Comment on the morphology of the erythrocytes.
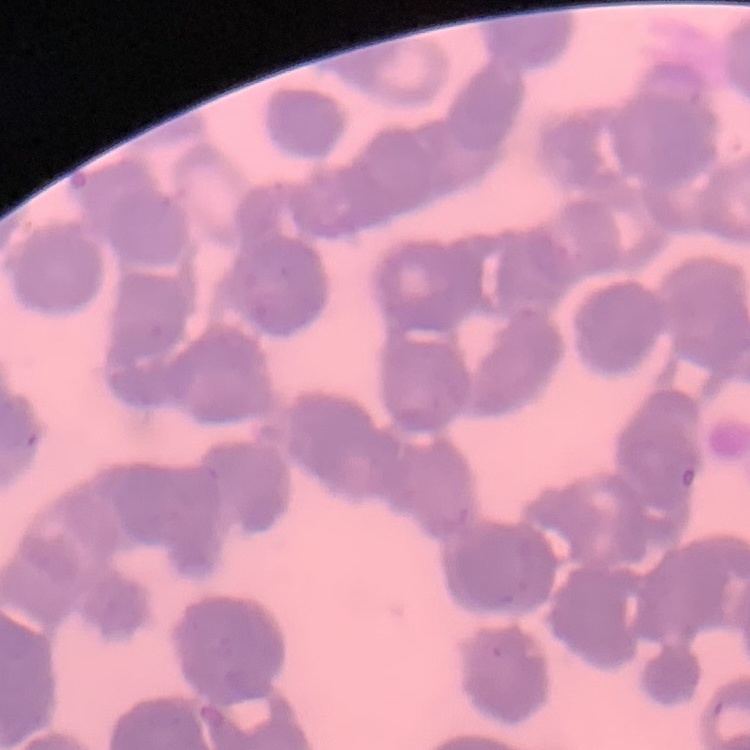
They show rouleaux formation.

Summary:
  - Stain: Field's or Giemsa
  - Image type: square crop of a larger photomicrograph
  - Preparation: thin blood film